Assess this cell for malaria.
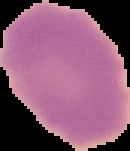

Uninfected.

image size = 130×151 pixels
image type = segmented cell region with the area outside set to black
preparation = thin blood film